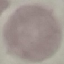
Summary:
  - Malaria status: uninfected
  - Preparation: thin blood smear
  - Capture: smartphone through the microscope eyepiece
  - Stain: Giemsa
  - Image type: cell patch, automatically extracted from a larger field of view and resized to 64 × 64 pixels